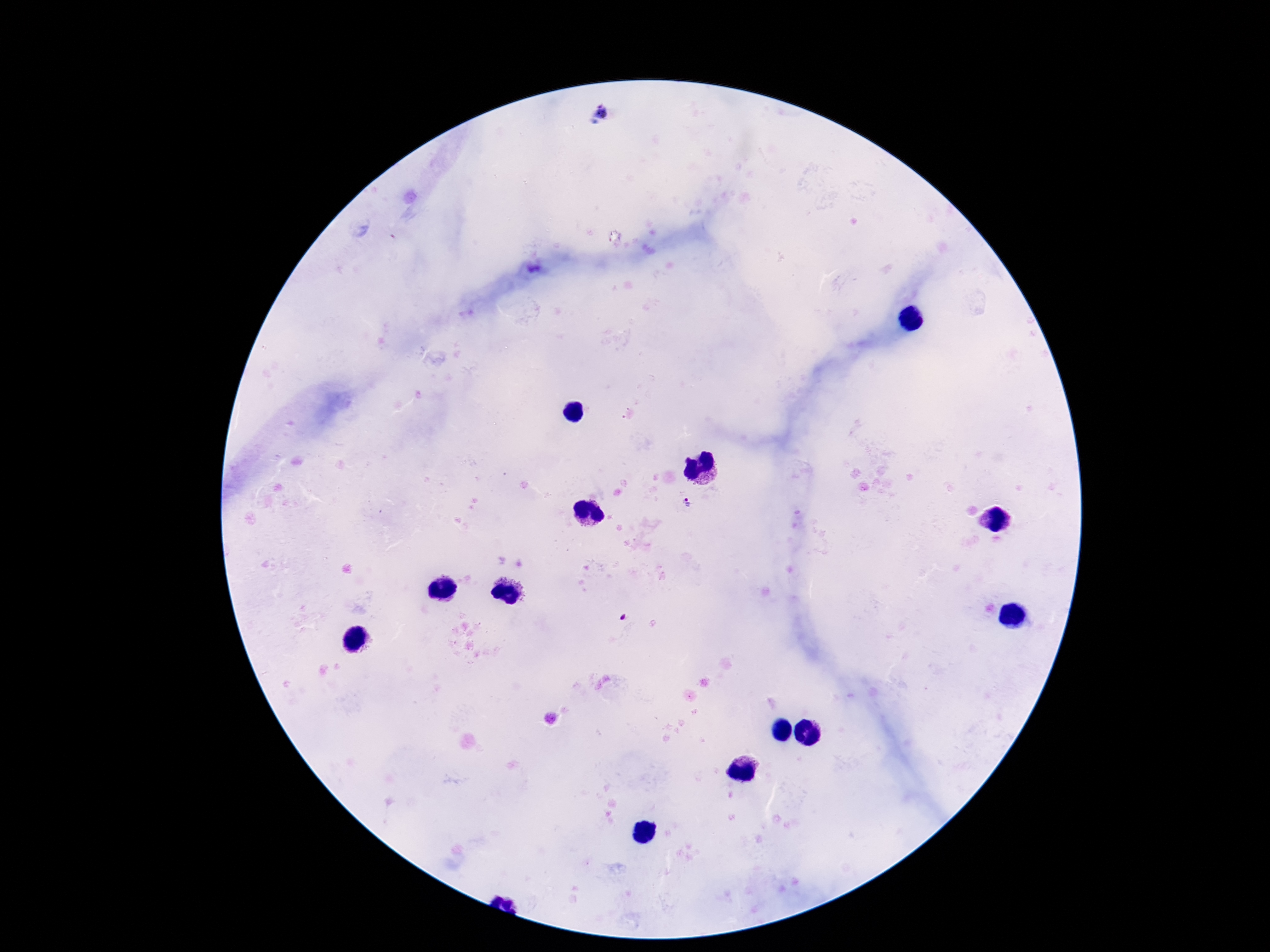
Approximate centers as {x, y} in pixels.
Summary:
  - Plasmodium parasite locations: {600, 115}, {687, 501}, {621, 618}
  - Patient malaria status: infected
  - Image size: 1270×952 pixels
  - Preparation: thick blood film
  - Stain: Giemsa
  - Magnification: 100x
  - Capture: smartphone camera through the microscope eyepiece
  - Field of view: single